Comment on the morphology of the erythrocytes.
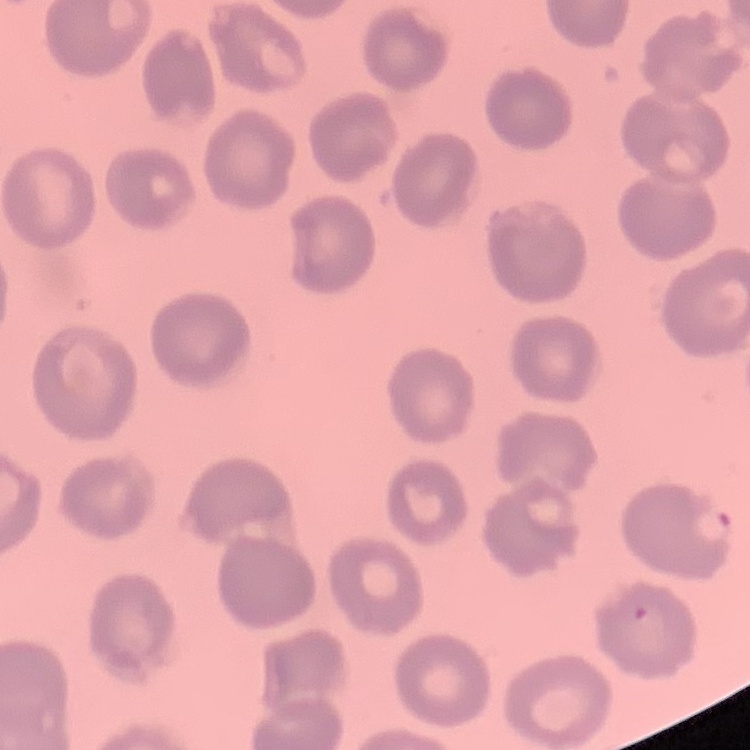

No rouleaux formation.

Field's or Giemsa stain. Thin peripheral smear. Square crop of a larger photomicrograph.